Point out each Plasmodium parasite.
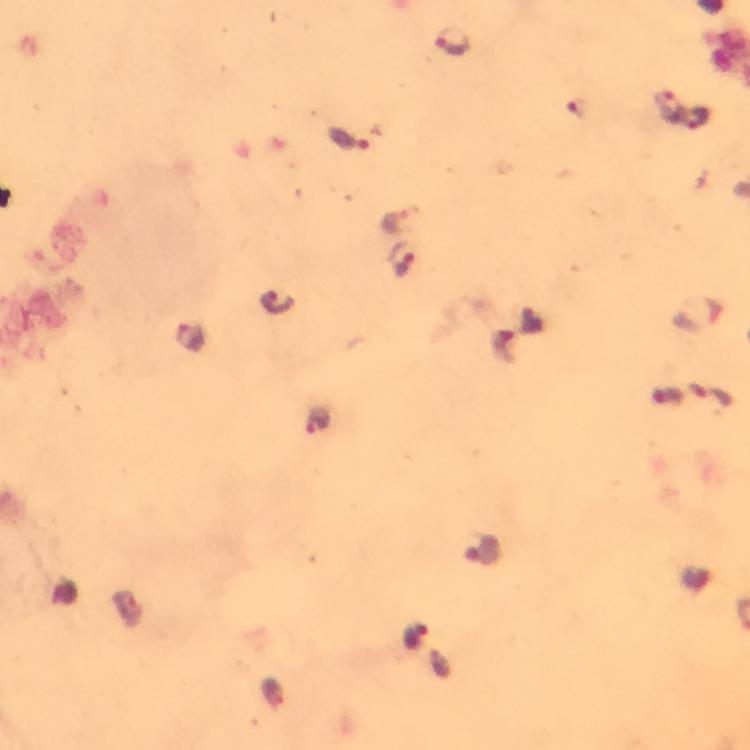

Approximate centers as (x, y) in pixels.
Plasmodium parasites: (452, 44), (668, 106), (695, 120), (348, 139), (402, 261), (276, 301), (190, 337), (715, 398), (317, 420), (416, 636).

At 100x magnification. From a malaria diagnostic workup. Giemsa-stained preparation. A crop from one field of view. Thick blood film. Image is 750×750 pixels. Immersion oil was used. Smartphone photograph taken through a microscope.